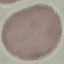 Result: no malaria parasites seen. Giemsa stain. Automatically extracted cell patch, resized to 64 × 64 pixels. Thin smear of blood. Acquired by smartphone through the microscope eyepiece.